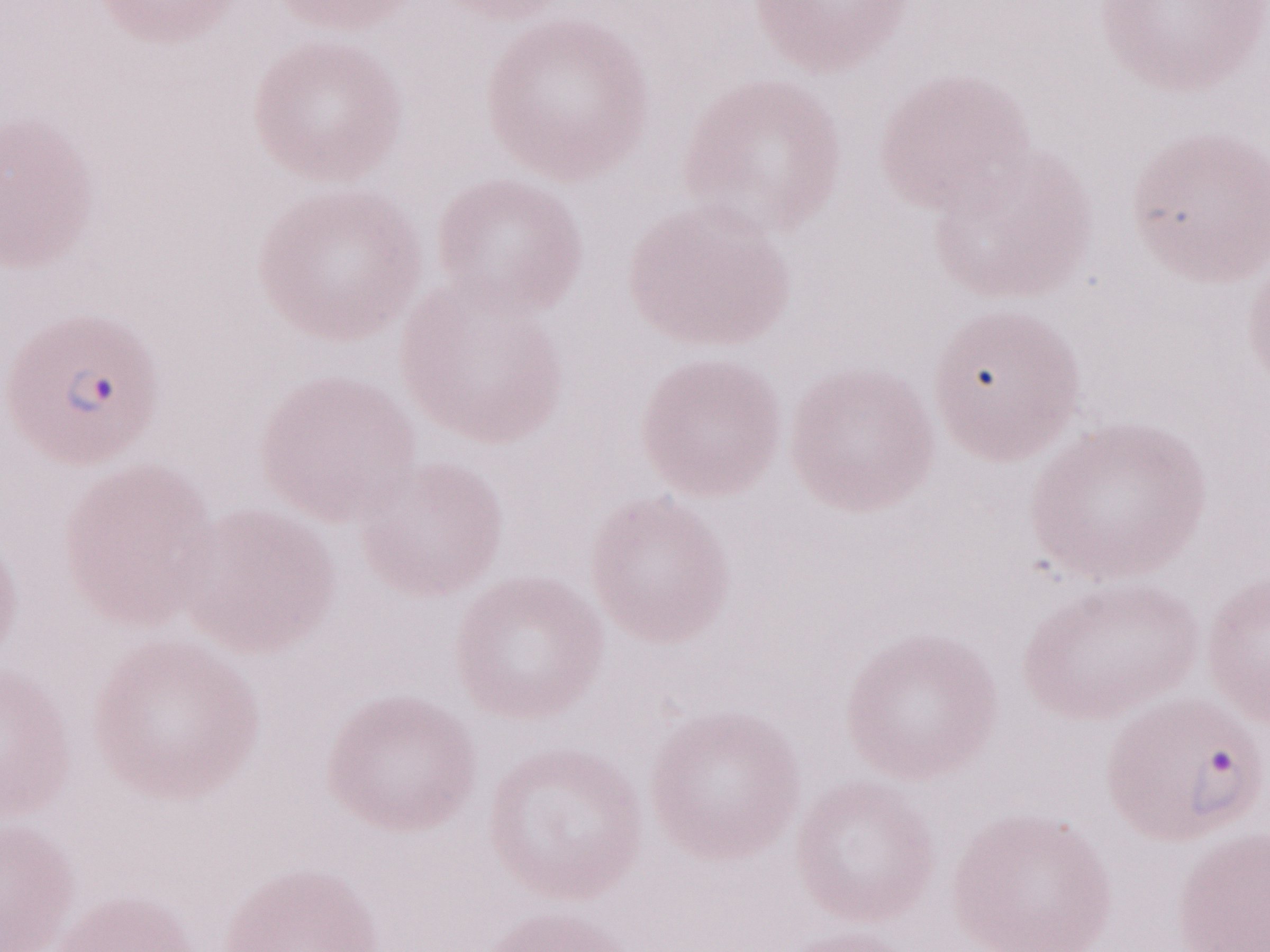 1,000x magnification. Image is 1270×952 pixels. Olympus BX43 microscope and DP73 digital camera. May-Grünwald-Giemsa-stained preparation. Single field of view. Thin blood smear. Malaria diagnosis (patient-level): positive.